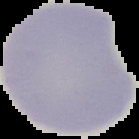

preparation = thin blood smear
malaria status = uninfected
image size = 139×139 pixels
image type = segmented cell region with the area outside set to black